Identify the blood parasite species.
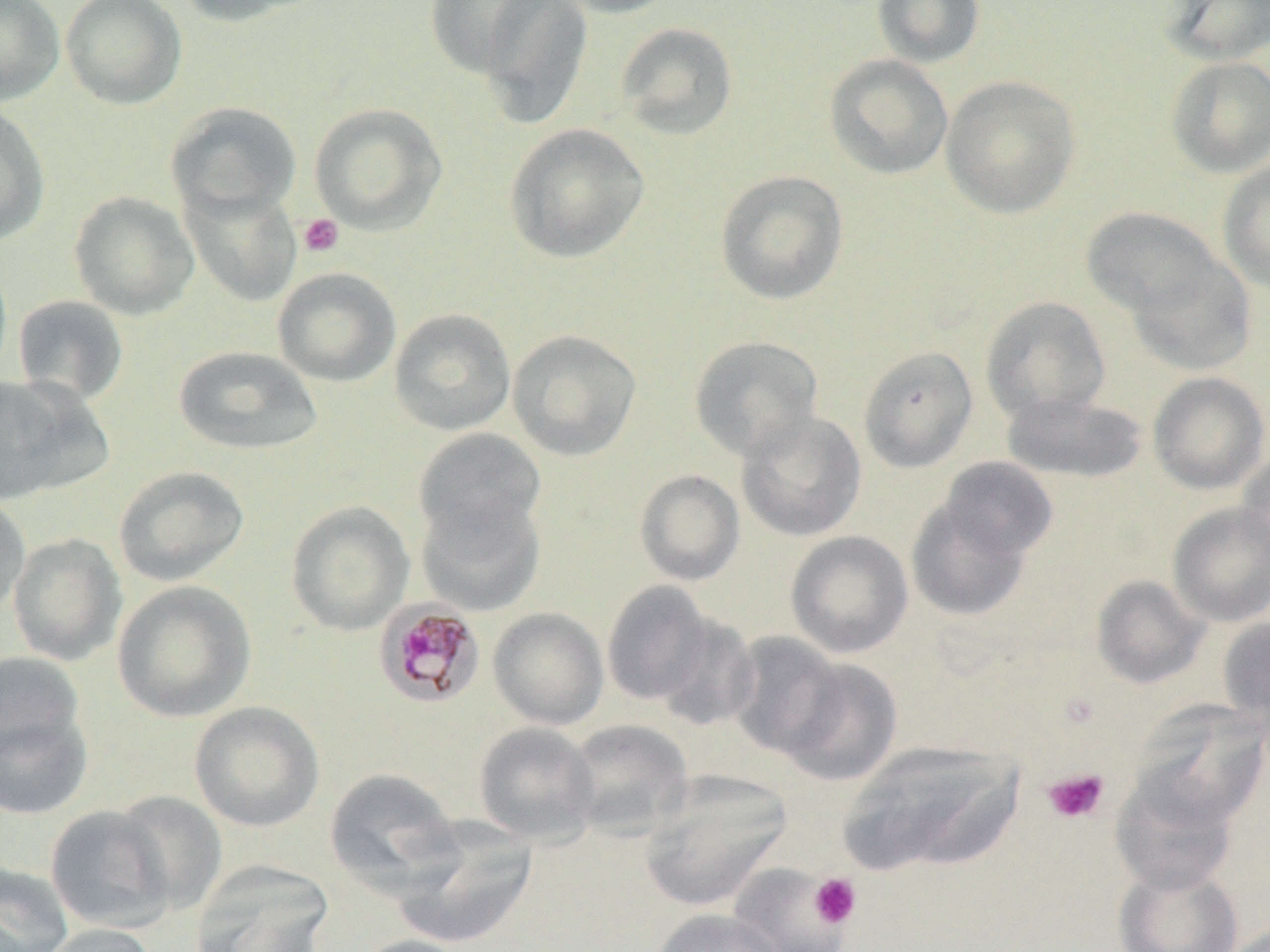

Plasmodium malariae.

Approximate bounding boxes as (x1, y1, x2, y2) in pixels. Plasmodium malariae-infected red blood cell locations: (377, 597, 489, 705). Uninfected red blood cell locations: (0, 0, 64, 106), (61, 0, 187, 110), (176, 0, 312, 26), (422, 0, 553, 81), (552, 0, 684, 18), (872, 0, 985, 67), (1162, 0, 1270, 63), (474, 1, 593, 129), (614, 22, 738, 140), (824, 54, 953, 180), (1165, 56, 1270, 178), (940, 75, 1081, 218), (165, 102, 302, 222), (309, 103, 447, 234), (0, 104, 51, 246), (503, 123, 650, 264), (1217, 161, 1270, 294), (715, 170, 849, 305), (181, 184, 302, 306), (68, 191, 200, 320), (1081, 207, 1219, 320), (1125, 250, 1256, 374), (272, 267, 402, 387), (12, 295, 129, 406), (981, 295, 1111, 424), (389, 308, 516, 436), (507, 329, 642, 461), (688, 335, 824, 461), (173, 345, 323, 456), (858, 346, 979, 473), (1147, 371, 1270, 494), (0, 375, 92, 504), (1002, 392, 1149, 483), (736, 410, 868, 542), (413, 428, 547, 546), (1235, 447, 1270, 566), (936, 457, 1058, 564), (112, 465, 250, 587), (634, 469, 745, 586), (415, 491, 546, 615), (0, 494, 31, 621), (906, 496, 1033, 622), (285, 500, 414, 635), (1167, 502, 1270, 627), (785, 530, 914, 658), (7, 532, 127, 666), (1091, 575, 1209, 688), (111, 580, 256, 722), (601, 581, 715, 705), (488, 607, 609, 730), (654, 614, 759, 730), (1216, 616, 1270, 731), (725, 631, 846, 758), (0, 650, 88, 775), (777, 657, 902, 785), (1131, 700, 1269, 829), (189, 701, 325, 832), (0, 704, 93, 819), (564, 719, 693, 839), (473, 721, 601, 846), (839, 740, 1024, 877), (324, 767, 462, 891), (639, 773, 791, 911), (1111, 773, 1239, 894), (111, 791, 227, 914), (45, 804, 175, 934), (393, 818, 538, 948), (189, 861, 334, 952), (0, 862, 74, 952), (727, 863, 851, 952), (1114, 863, 1244, 952), (649, 908, 787, 952), (35, 923, 159, 952), (350, 935, 479, 952). Platelet locations: (298, 214, 344, 257), (1042, 768, 1109, 823), (809, 873, 861, 928). Optical microscopy. May-Grünwald-Giemsa stain. Thin blood film. Single field of view. Captured at 1000x magnification. Image is 1270×952 pixels.